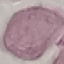

malaria_status: uninfected
capture: smartphone through the microscope eyepiece
preparation: thin smear
image_type: cell patch, automatically extracted from a larger field of view and resized to 64 × 64 pixels
stain: Giemsa